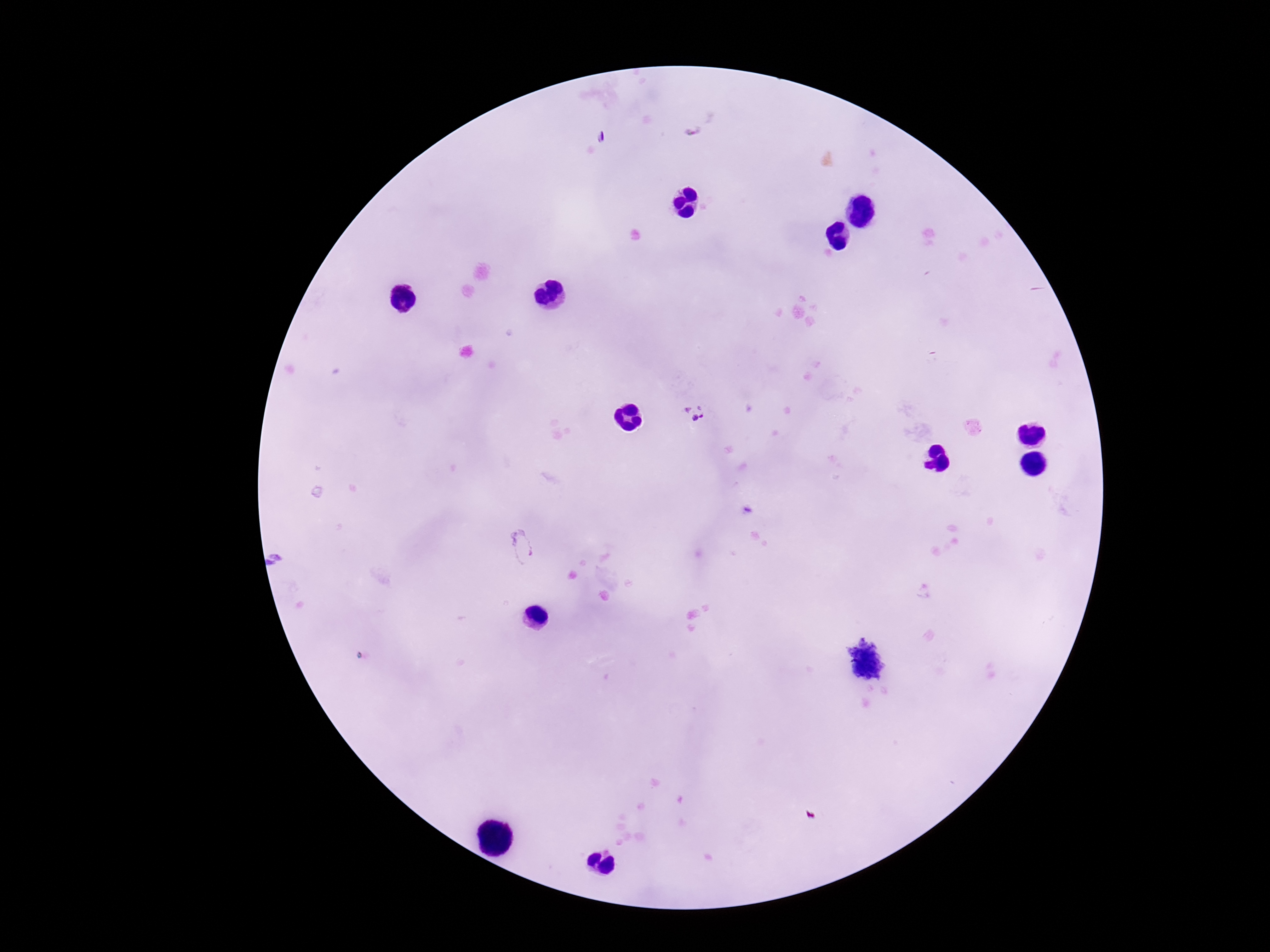
{
  "stain": "Giemsa",
  "preparation": "thick blood film",
  "image_size": "1270×952 pixels",
  "magnification": "100x",
  "field_of_view": "one from this slide",
  "patient_malaria_status": "infected",
  "capture": "smartphone camera through the microscope eyepiece",
  "plasmodium_parasite_locations": "approximate centers as [x, y] in pixels: [599, 137], [696, 412], [522, 545]"
}